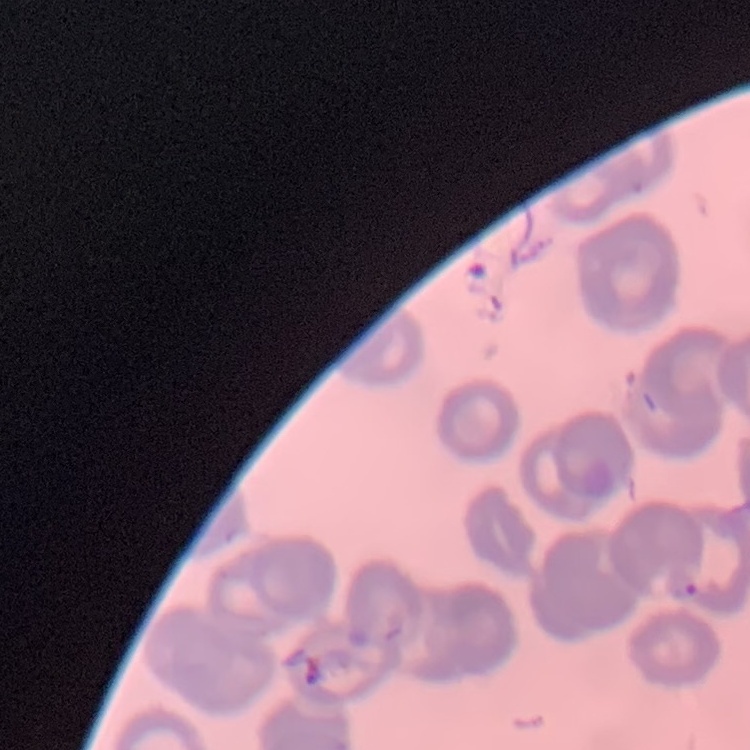
Summary:
  - Erythrocyte morphology: rouleaux formation
  - Stain: Field's or Giemsa
  - Image type: one tile cut from a larger photomicrograph
  - Preparation: thin peripheral smear